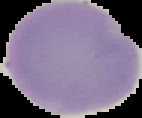
{
  "image_type": "segmented cell region with the area outside set to black",
  "image_size": "142×118 pixels",
  "malaria_status": "uninfected",
  "preparation": "thin blood film"
}